Report the malaria status of this cell.
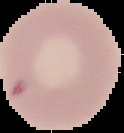

It is uninfected.

Summary:
  - Preparation: thin blood smear
  - Image type: segmented cell region on a black background
  - Image size: 124×133 pixels